Give the position of every Plasmodium parasite visible.
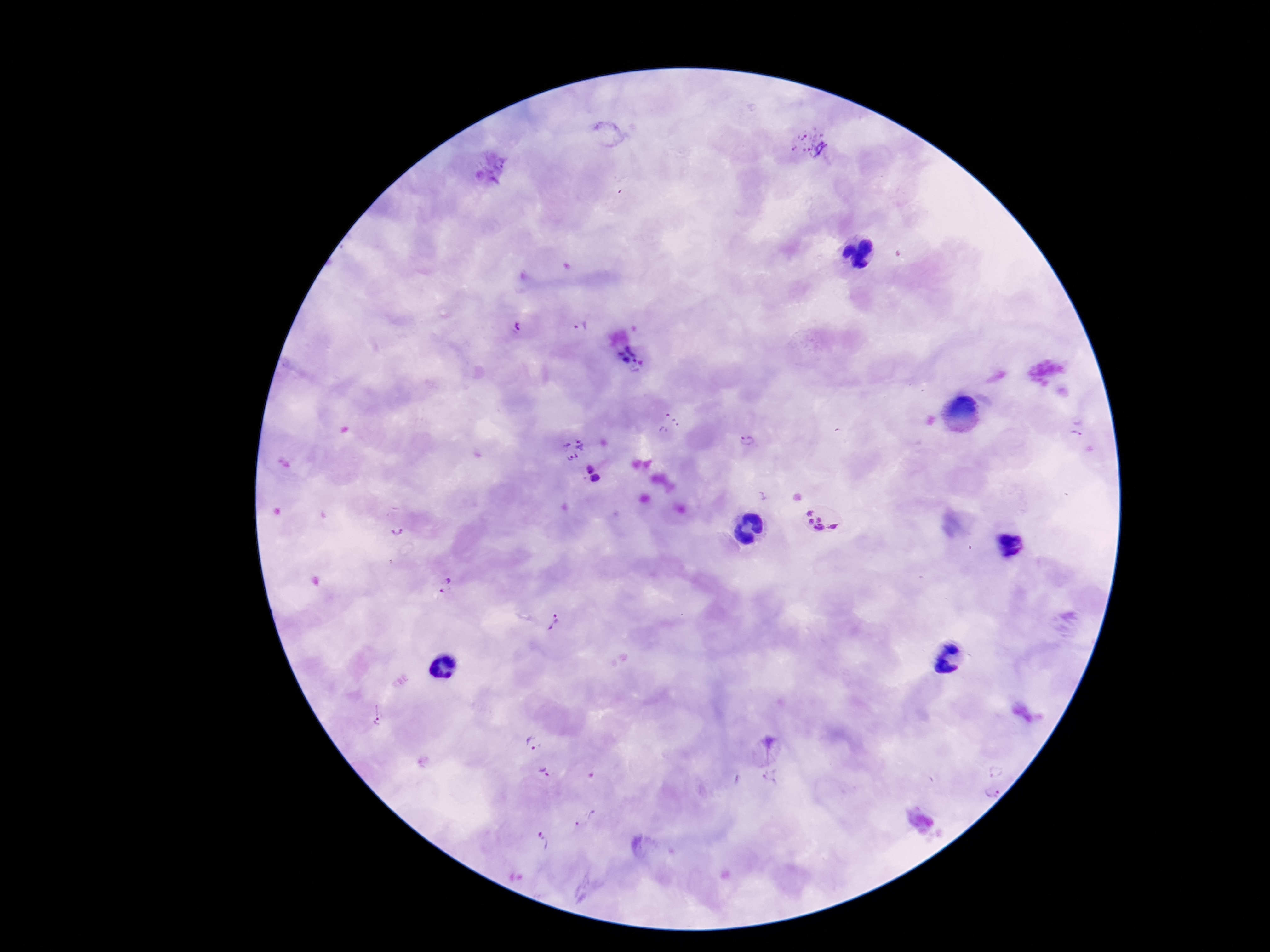

Approximate centers as (x, y) in pixels.
Plasmodium parasites: (809, 144), (581, 325), (519, 328), (625, 354), (638, 366), (670, 424), (1078, 427), (748, 441), (572, 448), (589, 469), (595, 479), (825, 519), (395, 533), (446, 585), (556, 624), (377, 715), (533, 743), (768, 749), (996, 769), (545, 774), (769, 778), (990, 793), (585, 819), (544, 842).

stain = Giemsa
capture = smartphone camera through the microscope eyepiece
magnification = 100x
preparation = thick blood smear
patient malaria status = positive
image size = 1270×952 pixels
field of view = one from this slide